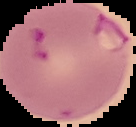
image size = 136×127 pixels
malaria status = parasitized
preparation = thin blood film
image type = segmented cell region with the area outside set to black